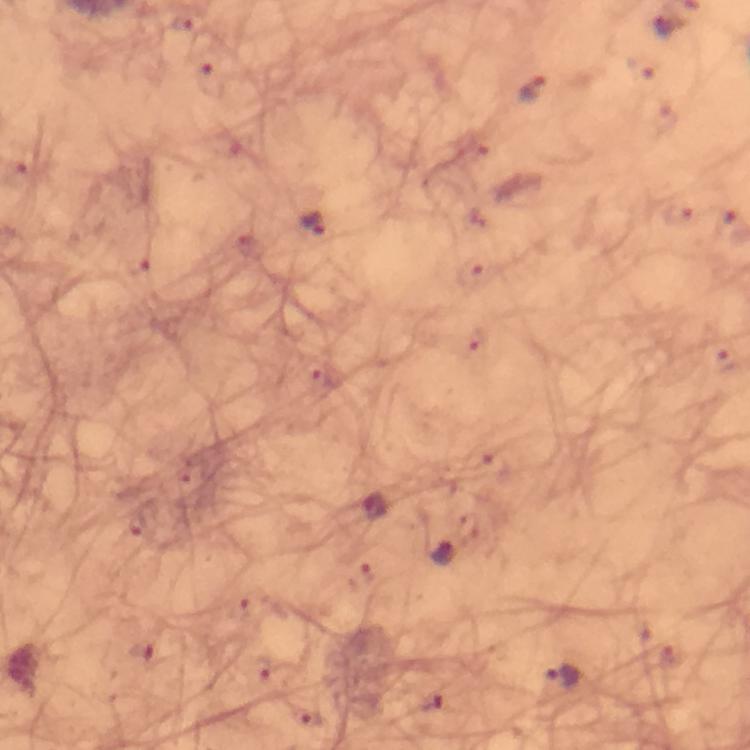
Approximate object centers, in pixels from the top-left corner.
Summary:
  - Plasmodium parasite locations: (x=182, y=24), (x=210, y=81), (x=531, y=90), (x=312, y=223), (x=375, y=508), (x=443, y=552), (x=562, y=676), (x=431, y=702)
  - Capture: smartphone mounted on the microscope
  - Cropped from: a single field of view
  - Stain: Giemsa
  - Image size: 750×750 pixels
  - Context: from a malaria diagnostic workup
  - Immersion oil: applied
  - Preparation: thick blood smear
  - Magnification: 100x